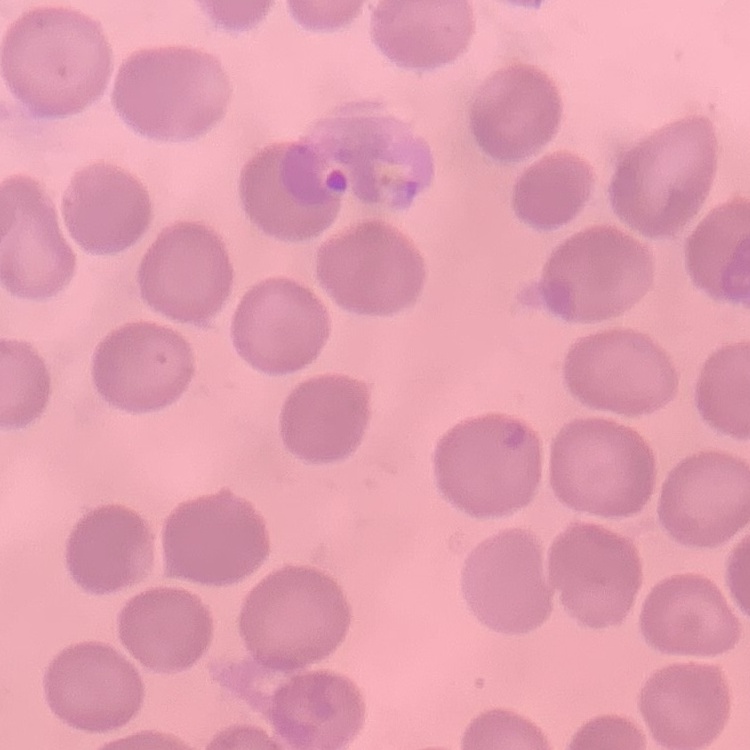
red blood cell morphology = no rouleaux formation
stain = Field's or Giemsa
image type = square crop of a larger photomicrograph
preparation = thin peripheral smear